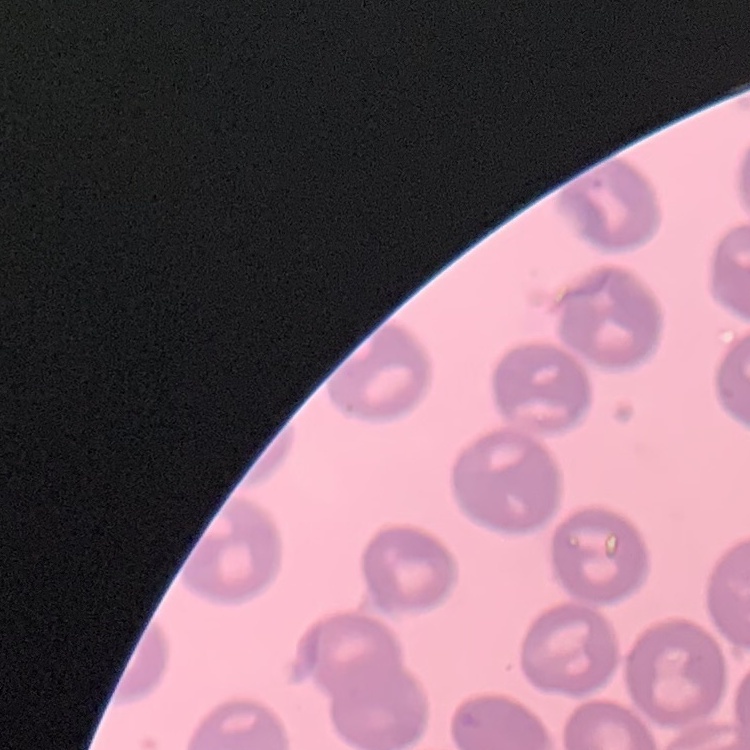
Summary:
  - Red blood cell morphology: no rouleaux formation
  - Image type: square crop of a larger photomicrograph
  - Preparation: thin blood film
  - Stain: Field's or Giemsa